Name the parasite shown.
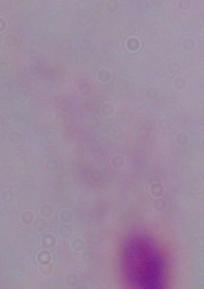
A trichomonad.

Summary:
  - Modality: micrograph
  - Magnification: 1000x